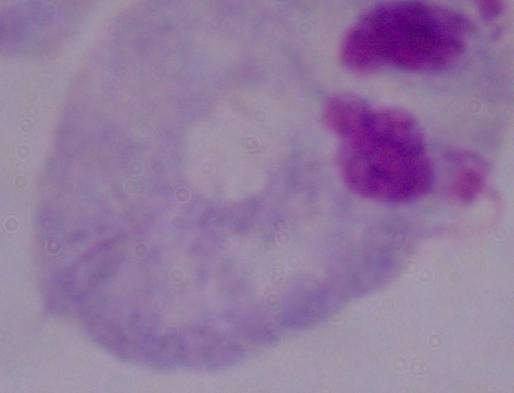
Captured at 1000x magnification. Photomicrograph. A trichomonad is seen.